Classify this cell by malaria status.
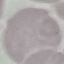

It is uninfected.

Thin smear of blood. Acquired by smartphone through the microscope eyepiece. Giemsa stain. Cell patch, automatically extracted from a larger field of view and resized to 64 × 64 pixels.